Classify this cell by malaria status.
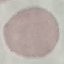

It is uninfected.

{
  "stain": "Giemsa",
  "capture": "smartphone through the microscope eyepiece",
  "image_type": "cell patch, automatically extracted from a larger field of view and resized to 64 × 64 pixels",
  "preparation": "thin blood film"
}